Describe the morphology of the erythrocytes.
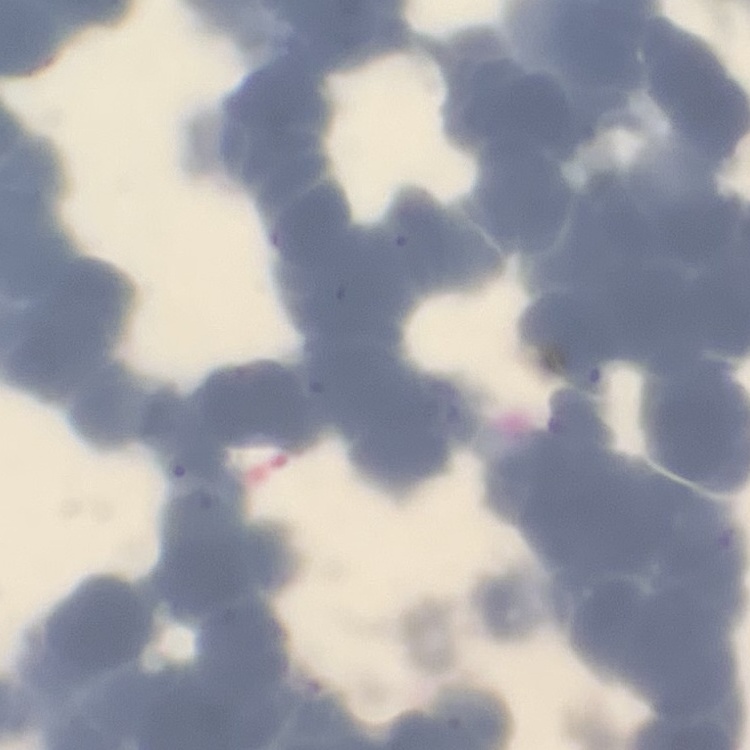

They show rouleaux formation.

image type = square crop of a larger photomicrograph
preparation = thin blood smear
stain = Field's or Giemsa